Describe the morphology of the red blood cells.
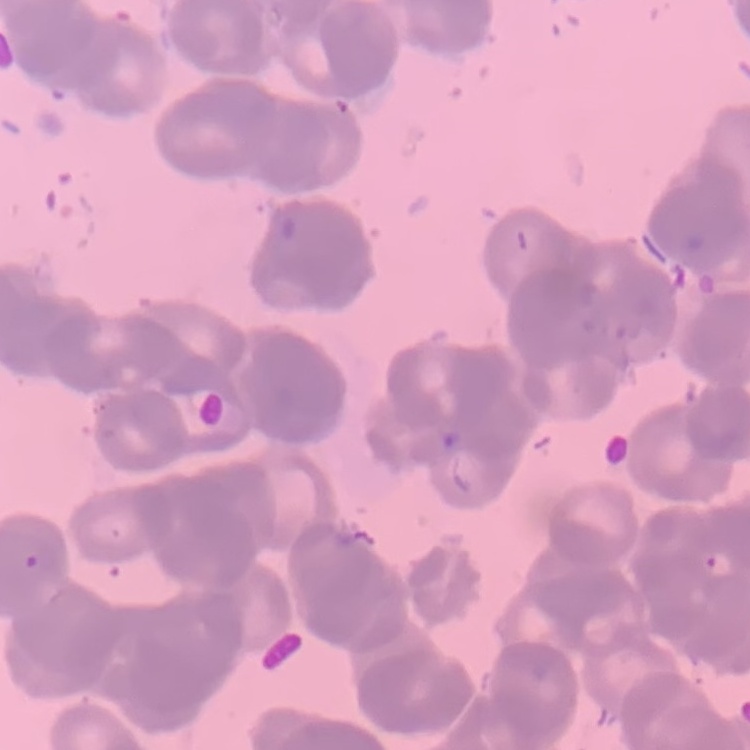
They show rouleaux formation.

preparation = thin blood film
stain = Field's or Giemsa
image type = square crop of a larger photomicrograph